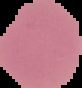

{
  "image_type": "segmented cell region on a black background",
  "result": "negative for malaria parasites",
  "image_size": "82×88 pixels",
  "preparation": "thin blood smear"
}